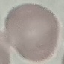
Summary:
  - Result: negative for malaria parasites
  - Stain: Giemsa
  - Image type: automatically extracted cell patch, resized to 64 × 64 pixels
  - Capture: smartphone camera at the microscope eyepiece
  - Preparation: thin blood smear